Give the extent of all uninfected red blood cells.
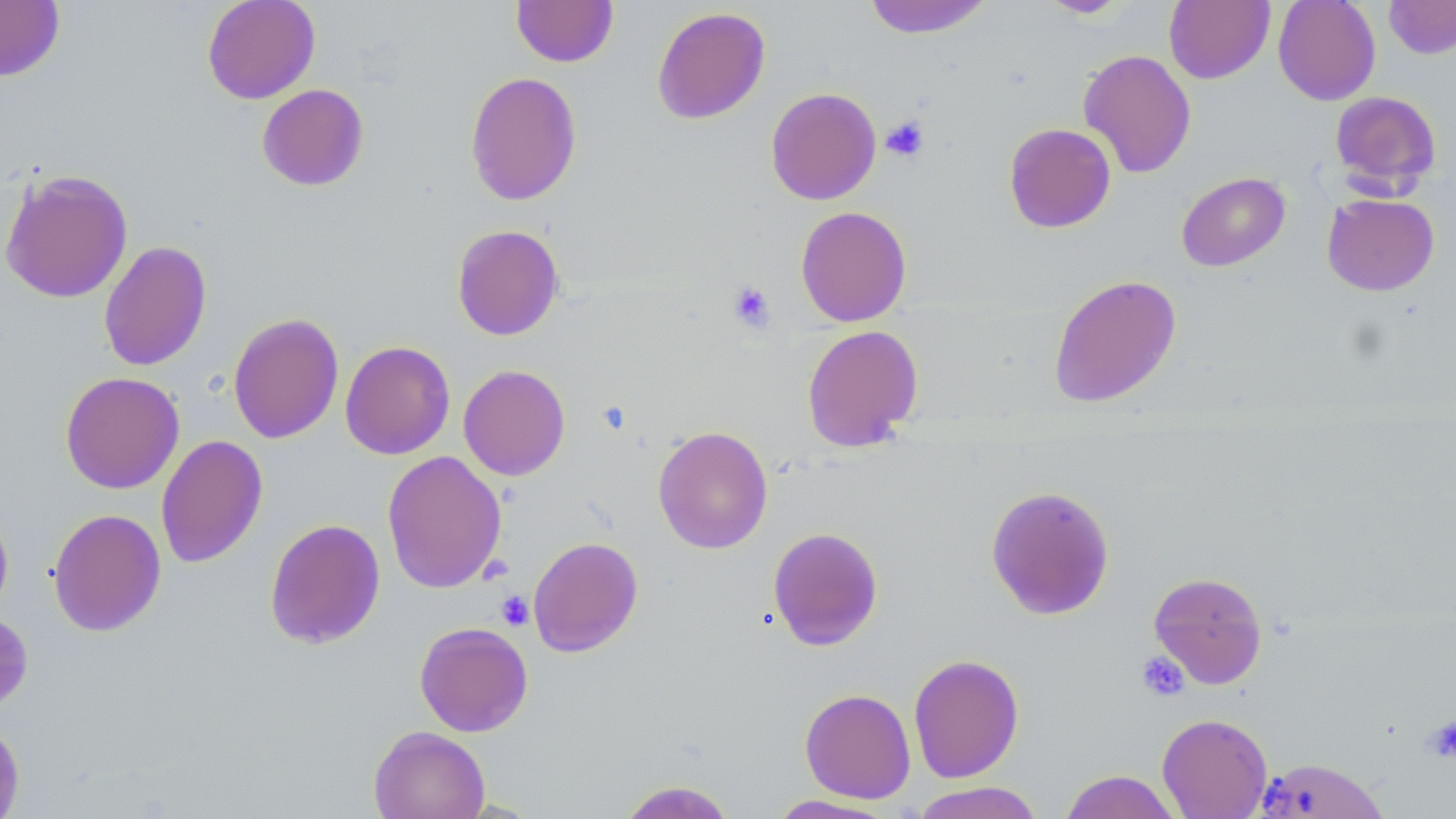
Approximate bounding boxes as [x1, y1, x2, y2] in pixels.
Uninfected red blood cells: [201, 0, 321, 104], [511, 0, 618, 67], [863, 0, 994, 38], [1038, 0, 1131, 18], [1164, 0, 1274, 84], [1273, 0, 1381, 105], [1384, 0, 1456, 59], [0, 1, 65, 81], [651, 6, 771, 125], [1078, 49, 1197, 179], [465, 71, 582, 206], [257, 84, 369, 191], [765, 86, 882, 205], [1330, 90, 1441, 193], [1003, 123, 1116, 233], [0, 168, 133, 303], [1176, 172, 1290, 271], [1321, 193, 1439, 296], [795, 206, 912, 327], [451, 224, 564, 341], [98, 240, 212, 372], [1048, 274, 1182, 408], [227, 312, 344, 444], [801, 324, 923, 452], [340, 340, 455, 459], [458, 364, 571, 480], [60, 371, 184, 494], [652, 425, 774, 554], [155, 434, 268, 568], [382, 450, 507, 594], [986, 484, 1115, 620], [0, 505, 14, 622], [47, 508, 166, 637], [264, 518, 385, 649], [768, 526, 884, 650], [528, 536, 643, 657], [1148, 571, 1268, 688], [414, 621, 533, 737], [908, 653, 1024, 783], [799, 687, 916, 803], [1157, 713, 1272, 818], [0, 718, 24, 819], [368, 725, 490, 819], [1255, 757, 1391, 818], [1059, 769, 1183, 819], [617, 779, 738, 818], [910, 781, 1045, 819], [764, 794, 901, 818].

slide-level diagnosis = no evidence of blood parasites
stain = May-Grünwald-Giemsa
preparation = thin blood film
modality = light microscopy
magnification = 1000x
field of view = single
image size = 1456×819 pixels
platelet locations = approximate bounding boxes as [x1, y1, x2, y2] in pixels: [881, 115, 929, 162], [728, 281, 776, 332], [496, 591, 534, 630], [1136, 651, 1189, 702], [1422, 715, 1456, 763]